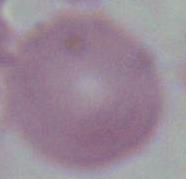
Summary:
  - Modality: photomicrograph
  - Magnification: 1000x
  - Identification: erythrocyte